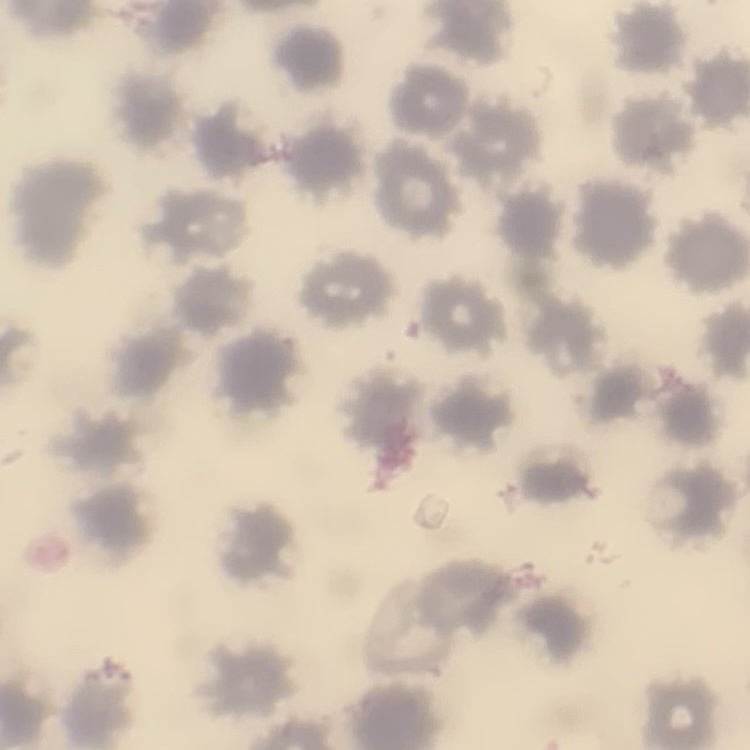

red blood cell morphology = no rouleaux formation
stain = Field's or Giemsa
preparation = thin peripheral smear
image type = one tile cut from a larger photomicrograph